Classify this cell by malaria status.
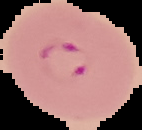

It is parasitized.

Summary:
  - Image size: 142×130 pixels
  - Preparation: thin blood film
  - Image type: segmented cell region on a black background